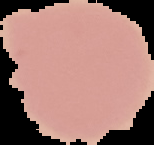
Summary:
  - Malaria status: uninfected
  - Image size: 154×145 pixels
  - Image type: segmented cell region with the area outside set to black
  - Preparation: thin blood smear